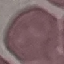

result = no malaria parasites seen
capture = smartphone through the microscope eyepiece
stain = Giemsa
preparation = thin blood smear
image type = cell patch, automatically extracted from a larger field of view and resized to 64 × 64 pixels